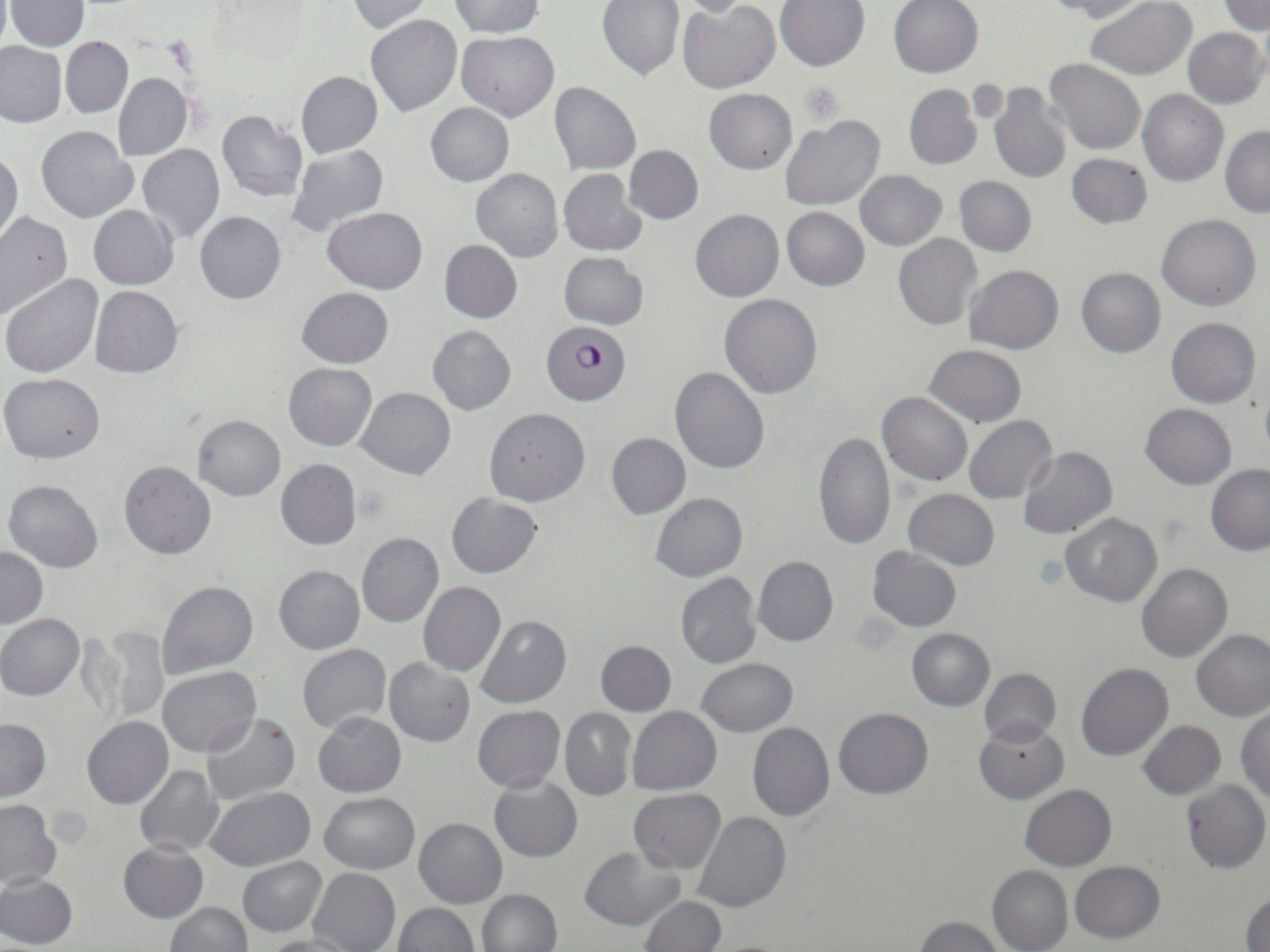

slide-level diagnosis = Plasmodium falciparum
image size = 1270×952 pixels
modality = optical microscopy
Plasmodium falciparum-infected red blood cell locations = approximate bounding boxes as named x1/y1/x2/y2 corners in pixels: (x1=540, y1=321, x2=631, y2=405)
field of view = one of a larger specimen
uninfected red blood cell locations = approximate bounding boxes as named x1/y1/x2/y2 corners in pixels: (x1=448, y1=0, x2=545, y2=38), (x1=450, y1=0, x2=548, y2=87), (x1=598, y1=0, x2=684, y2=79), (x1=672, y1=0, x2=756, y2=16), (x1=888, y1=0, x2=983, y2=78), (x1=1042, y1=0, x2=1148, y2=22), (x1=1086, y1=0, x2=1196, y2=80), (x1=1218, y1=0, x2=1269, y2=35), (x1=6, y1=1, x2=89, y2=51), (x1=347, y1=1, x2=434, y2=33), (x1=774, y1=1, x2=869, y2=72), (x1=678, y1=4, x2=780, y2=93), (x1=367, y1=15, x2=462, y2=116), (x1=1182, y1=27, x2=1269, y2=108), (x1=455, y1=31, x2=560, y2=121), (x1=60, y1=37, x2=133, y2=118), (x1=0, y1=41, x2=67, y2=127), (x1=1044, y1=58, x2=1148, y2=155), (x1=296, y1=71, x2=381, y2=158), (x1=113, y1=73, x2=193, y2=160), (x1=987, y1=81, x2=1071, y2=183), (x1=550, y1=82, x2=641, y2=174), (x1=904, y1=84, x2=981, y2=170), (x1=703, y1=88, x2=797, y2=174), (x1=1138, y1=89, x2=1229, y2=187), (x1=426, y1=103, x2=513, y2=185), (x1=217, y1=111, x2=308, y2=201), (x1=781, y1=116, x2=886, y2=211), (x1=37, y1=125, x2=139, y2=222), (x1=1220, y1=126, x2=1270, y2=216), (x1=137, y1=144, x2=225, y2=243), (x1=287, y1=145, x2=389, y2=238), (x1=623, y1=145, x2=703, y2=225), (x1=0, y1=150, x2=22, y2=247), (x1=1066, y1=153, x2=1152, y2=228), (x1=471, y1=168, x2=563, y2=262), (x1=558, y1=169, x2=647, y2=256), (x1=855, y1=170, x2=947, y2=250), (x1=954, y1=176, x2=1036, y2=257), (x1=88, y1=206, x2=178, y2=289), (x1=324, y1=207, x2=427, y2=293), (x1=782, y1=207, x2=870, y2=291), (x1=691, y1=209, x2=784, y2=302), (x1=194, y1=211, x2=286, y2=304), (x1=0, y1=212, x2=73, y2=320), (x1=1156, y1=214, x2=1262, y2=311), (x1=894, y1=233, x2=983, y2=331), (x1=438, y1=240, x2=522, y2=323), (x1=559, y1=250, x2=649, y2=329), (x1=964, y1=265, x2=1062, y2=354), (x1=1076, y1=268, x2=1165, y2=357), (x1=1, y1=275, x2=104, y2=378), (x1=90, y1=286, x2=184, y2=378), (x1=297, y1=287, x2=393, y2=368), (x1=719, y1=292, x2=823, y2=398), (x1=1165, y1=317, x2=1261, y2=408), (x1=428, y1=325, x2=517, y2=415), (x1=924, y1=344, x2=1026, y2=427), (x1=283, y1=363, x2=377, y2=452), (x1=669, y1=366, x2=770, y2=474), (x1=0, y1=372, x2=106, y2=463), (x1=357, y1=387, x2=456, y2=480), (x1=1260, y1=389, x2=1270, y2=466), (x1=877, y1=392, x2=973, y2=486), (x1=1141, y1=403, x2=1236, y2=488), (x1=483, y1=406, x2=590, y2=505), (x1=193, y1=414, x2=285, y2=500), (x1=964, y1=415, x2=1057, y2=504), (x1=812, y1=430, x2=896, y2=551), (x1=606, y1=432, x2=691, y2=519), (x1=1018, y1=446, x2=1116, y2=539), (x1=276, y1=458, x2=363, y2=550), (x1=118, y1=460, x2=217, y2=560), (x1=1205, y1=464, x2=1270, y2=555), (x1=4, y1=479, x2=104, y2=573), (x1=902, y1=489, x2=999, y2=569), (x1=651, y1=492, x2=748, y2=581), (x1=446, y1=493, x2=544, y2=578), (x1=1061, y1=512, x2=1161, y2=607), (x1=356, y1=532, x2=445, y2=628), (x1=0, y1=546, x2=48, y2=628), (x1=867, y1=546, x2=962, y2=631), (x1=752, y1=556, x2=838, y2=647), (x1=1136, y1=561, x2=1232, y2=662), (x1=274, y1=565, x2=365, y2=653), (x1=674, y1=572, x2=761, y2=670), (x1=155, y1=580, x2=259, y2=681), (x1=418, y1=581, x2=507, y2=677), (x1=0, y1=614, x2=84, y2=700), (x1=475, y1=615, x2=571, y2=709), (x1=98, y1=626, x2=169, y2=722), (x1=906, y1=628, x2=994, y2=711), (x1=1191, y1=628, x2=1270, y2=721), (x1=595, y1=640, x2=676, y2=715), (x1=297, y1=643, x2=390, y2=732), (x1=383, y1=657, x2=474, y2=746), (x1=696, y1=657, x2=798, y2=737), (x1=1075, y1=662, x2=1173, y2=760), (x1=157, y1=665, x2=261, y2=757), (x1=980, y1=668, x2=1061, y2=746), (x1=473, y1=705, x2=565, y2=793), (x1=1237, y1=705, x2=1269, y2=802), (x1=560, y1=707, x2=636, y2=801), (x1=628, y1=707, x2=722, y2=794), (x1=833, y1=707, x2=933, y2=799), (x1=313, y1=712, x2=405, y2=797), (x1=201, y1=713, x2=300, y2=805), (x1=0, y1=717, x2=50, y2=801), (x1=82, y1=717, x2=173, y2=809), (x1=974, y1=719, x2=1068, y2=803), (x1=1137, y1=720, x2=1225, y2=798), (x1=747, y1=722, x2=834, y2=821), (x1=134, y1=764, x2=223, y2=857), (x1=489, y1=776, x2=582, y2=862), (x1=1181, y1=778, x2=1270, y2=872), (x1=1020, y1=784, x2=1115, y2=871), (x1=206, y1=787, x2=317, y2=870), (x1=629, y1=788, x2=725, y2=873), (x1=319, y1=791, x2=419, y2=872), (x1=0, y1=800, x2=61, y2=890), (x1=692, y1=811, x2=791, y2=913), (x1=414, y1=818, x2=507, y2=907), (x1=117, y1=841, x2=208, y2=922), (x1=580, y1=846, x2=682, y2=931), (x1=237, y1=856, x2=327, y2=936), (x1=1069, y1=860, x2=1164, y2=942), (x1=987, y1=864, x2=1073, y2=952), (x1=309, y1=867, x2=399, y2=952), (x1=0, y1=872, x2=77, y2=948), (x1=476, y1=888, x2=562, y2=952), (x1=1243, y1=891, x2=1270, y2=952), (x1=640, y1=896, x2=725, y2=952), (x1=165, y1=902, x2=252, y2=952), (x1=394, y1=902, x2=479, y2=951), (x1=916, y1=915, x2=1004, y2=952), (x1=261, y1=935, x2=357, y2=952)
preparation = thin blood film
stain = May-Grünwald-Giemsa
platelet locations = approximate bounding boxes as named x1/y1/x2/y2 corners in pixels: (x1=799, y1=81, x2=845, y2=125)
magnification = 1000x